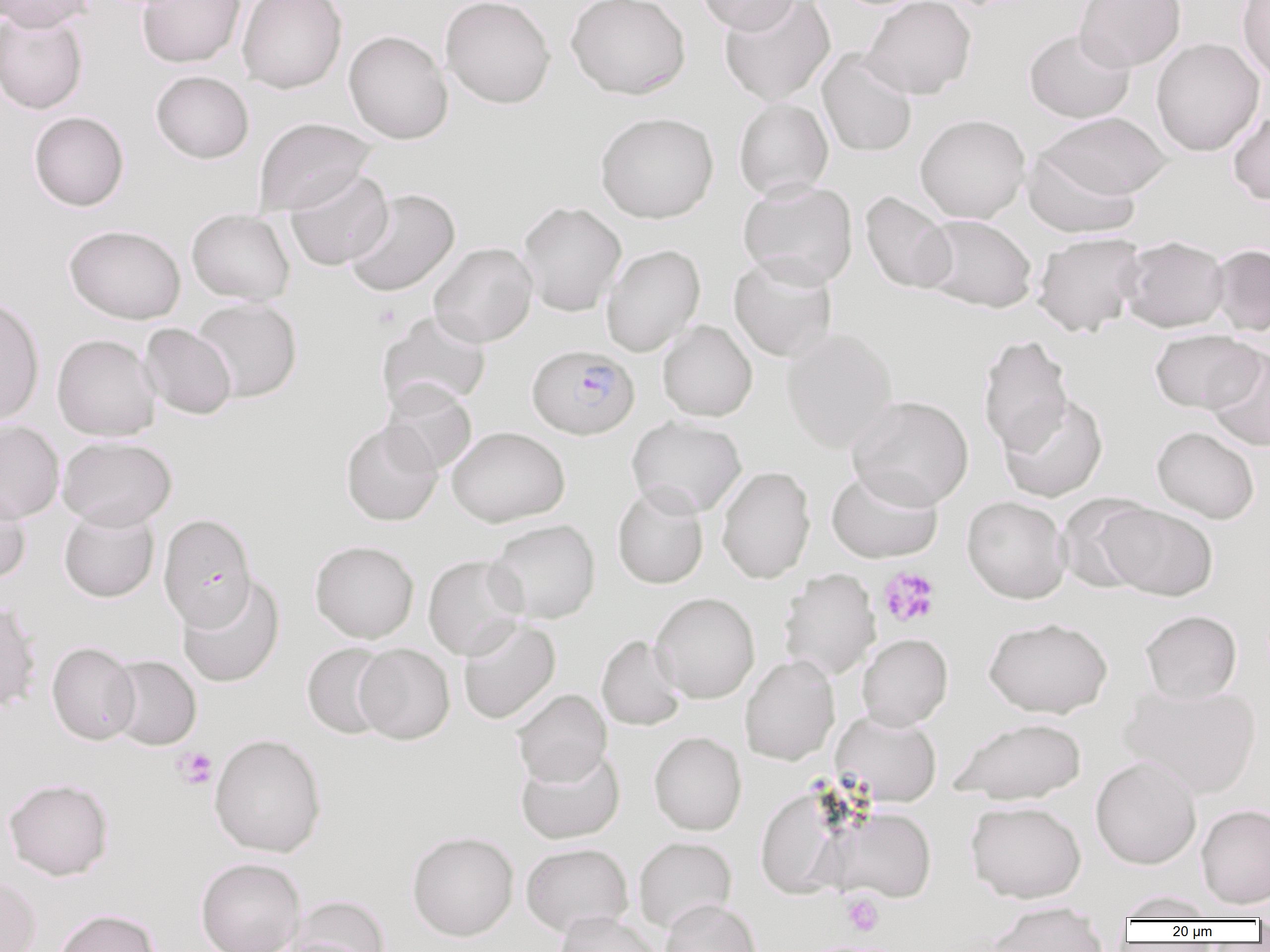 Approximate bounding boxes as named x1/y1/x2/y2 corners in pixels. Platelet locations: (x1=371, y1=304, x2=400, y2=329), (x1=877, y1=567, x2=940, y2=628), (x1=174, y1=747, x2=218, y2=789), (x1=842, y1=894, x2=883, y2=937). Uninfected red blood cell locations: (x1=137, y1=0, x2=245, y2=68), (x1=237, y1=0, x2=347, y2=93), (x1=440, y1=0, x2=556, y2=109), (x1=566, y1=0, x2=691, y2=99), (x1=696, y1=0, x2=802, y2=35), (x1=719, y1=0, x2=835, y2=105), (x1=861, y1=0, x2=976, y2=100), (x1=1075, y1=0, x2=1186, y2=72), (x1=1237, y1=0, x2=1270, y2=82), (x1=0, y1=1, x2=96, y2=31), (x1=0, y1=9, x2=89, y2=114), (x1=1024, y1=28, x2=1135, y2=123), (x1=343, y1=30, x2=453, y2=144), (x1=1151, y1=37, x2=1264, y2=156), (x1=817, y1=49, x2=918, y2=157), (x1=151, y1=71, x2=254, y2=163), (x1=734, y1=98, x2=834, y2=201), (x1=1227, y1=109, x2=1270, y2=205), (x1=28, y1=111, x2=129, y2=211), (x1=595, y1=112, x2=719, y2=223), (x1=1039, y1=112, x2=1173, y2=200), (x1=914, y1=114, x2=1030, y2=223), (x1=254, y1=117, x2=376, y2=216), (x1=1022, y1=147, x2=1142, y2=238), (x1=285, y1=168, x2=393, y2=270), (x1=737, y1=179, x2=858, y2=289), (x1=344, y1=188, x2=460, y2=297), (x1=860, y1=191, x2=956, y2=294), (x1=517, y1=201, x2=627, y2=316), (x1=186, y1=208, x2=295, y2=305), (x1=920, y1=214, x2=1038, y2=312), (x1=64, y1=224, x2=186, y2=324), (x1=1032, y1=232, x2=1147, y2=337), (x1=1118, y1=236, x2=1230, y2=332), (x1=429, y1=242, x2=538, y2=347), (x1=601, y1=244, x2=705, y2=357), (x1=1210, y1=244, x2=1269, y2=336), (x1=729, y1=253, x2=838, y2=361), (x1=0, y1=296, x2=44, y2=426), (x1=191, y1=298, x2=302, y2=402), (x1=376, y1=310, x2=492, y2=413), (x1=657, y1=320, x2=757, y2=422), (x1=139, y1=323, x2=237, y2=419), (x1=781, y1=327, x2=898, y2=453), (x1=1149, y1=329, x2=1263, y2=413), (x1=52, y1=334, x2=161, y2=441), (x1=977, y1=335, x2=1074, y2=456), (x1=1205, y1=346, x2=1270, y2=452), (x1=381, y1=381, x2=477, y2=476), (x1=847, y1=395, x2=974, y2=510), (x1=999, y1=395, x2=1108, y2=502), (x1=626, y1=415, x2=747, y2=518), (x1=0, y1=420, x2=64, y2=523), (x1=340, y1=420, x2=443, y2=526), (x1=446, y1=426, x2=570, y2=527), (x1=1151, y1=426, x2=1260, y2=524), (x1=57, y1=436, x2=177, y2=530), (x1=717, y1=466, x2=815, y2=584), (x1=826, y1=467, x2=943, y2=563), (x1=612, y1=483, x2=709, y2=589), (x1=0, y1=485, x2=31, y2=585), (x1=1057, y1=493, x2=1159, y2=594), (x1=962, y1=496, x2=1071, y2=604), (x1=1102, y1=503, x2=1218, y2=600), (x1=58, y1=507, x2=160, y2=603), (x1=486, y1=519, x2=601, y2=624), (x1=310, y1=540, x2=419, y2=643), (x1=423, y1=554, x2=527, y2=660), (x1=778, y1=568, x2=881, y2=681), (x1=177, y1=575, x2=284, y2=688), (x1=650, y1=592, x2=760, y2=704), (x1=0, y1=599, x2=41, y2=714), (x1=1140, y1=610, x2=1242, y2=703), (x1=983, y1=617, x2=1113, y2=718), (x1=457, y1=618, x2=560, y2=725), (x1=856, y1=633, x2=953, y2=731), (x1=596, y1=634, x2=686, y2=731), (x1=46, y1=642, x2=140, y2=745), (x1=302, y1=642, x2=394, y2=739), (x1=354, y1=643, x2=454, y2=744), (x1=739, y1=654, x2=840, y2=765), (x1=106, y1=655, x2=201, y2=750), (x1=1120, y1=682, x2=1262, y2=798), (x1=512, y1=689, x2=611, y2=786), (x1=831, y1=710, x2=942, y2=806), (x1=950, y1=717, x2=1087, y2=804), (x1=648, y1=731, x2=746, y2=835), (x1=208, y1=733, x2=327, y2=858), (x1=515, y1=747, x2=625, y2=844), (x1=1090, y1=756, x2=1202, y2=869), (x1=3, y1=778, x2=113, y2=880), (x1=755, y1=787, x2=850, y2=899), (x1=965, y1=800, x2=1086, y2=903), (x1=1196, y1=804, x2=1270, y2=909), (x1=822, y1=806, x2=937, y2=902), (x1=406, y1=831, x2=519, y2=941), (x1=633, y1=836, x2=737, y2=933), (x1=521, y1=842, x2=634, y2=936), (x1=195, y1=857, x2=306, y2=952), (x1=0, y1=875, x2=41, y2=952), (x1=1114, y1=891, x2=1221, y2=920), (x1=290, y1=895, x2=390, y2=951), (x1=660, y1=898, x2=760, y2=952), (x1=986, y1=907, x2=1110, y2=951), (x1=52, y1=909, x2=160, y2=952), (x1=555, y1=910, x2=662, y2=952), (x1=805, y1=939, x2=904, y2=952). Plasmodium falciparum-infected red blood cell locations: (x1=527, y1=344, x2=639, y2=439), (x1=158, y1=514, x2=256, y2=630). Slide-level diagnosis: Plasmodium falciparum. Single field of view. Image is 1270×952 pixels. Light microscopy. Captured at 1000x magnification. Thin blood smear.